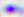

{
  "modality": "micrograph",
  "magnification": "400x",
  "identification": "Toxoplasma gondii"
}